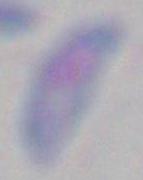
identification = Toxoplasma gondii
modality = micrograph
magnification = 1000x